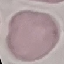

{
  "malaria_status": "uninfected",
  "image_type": "cell patch, automatically extracted from a larger field of view and resized to 64 × 64 pixels",
  "preparation": "thin smear",
  "capture": "smartphone through the microscope eyepiece",
  "stain": "Giemsa"
}